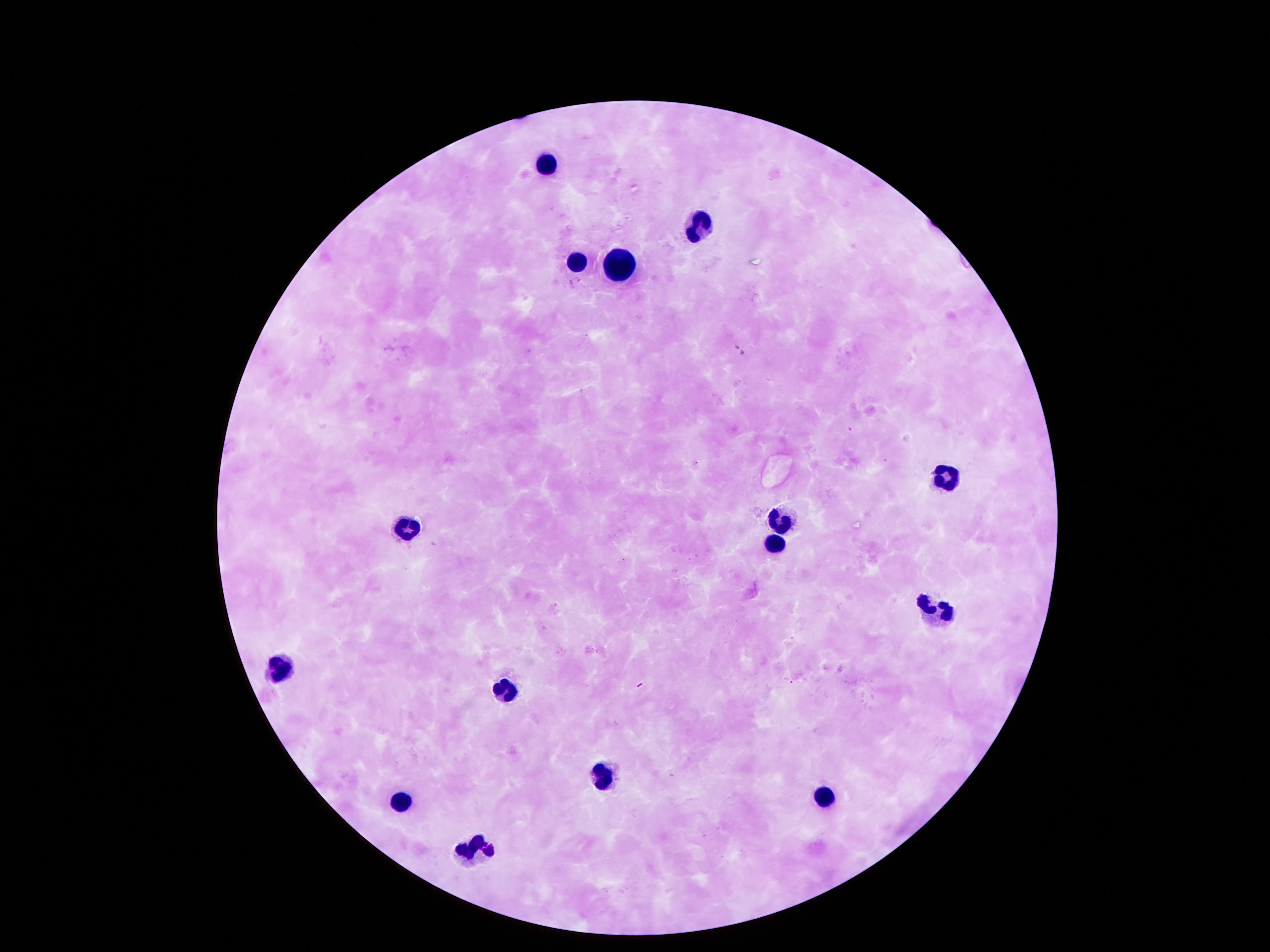

leukocyte locations = approximate centers as {x, y} in pixels: {548, 161}, {693, 225}, {619, 259}, {575, 262}, {941, 477}, {783, 516}, {407, 520}, {770, 541}, {945, 605}, {282, 665}, {504, 689}, {605, 773}, {820, 792}, {403, 800}, {467, 847}
magnification = 100x
patient malaria status = not infected
field of view = one from this slide
image size = 1270×952 pixels
preparation = thick peripheral-blood smear
capture = smartphone camera through the microscope eyepiece
stain = Giemsa